Give the extent of all Plasmodium malariae-infected red blood cells.
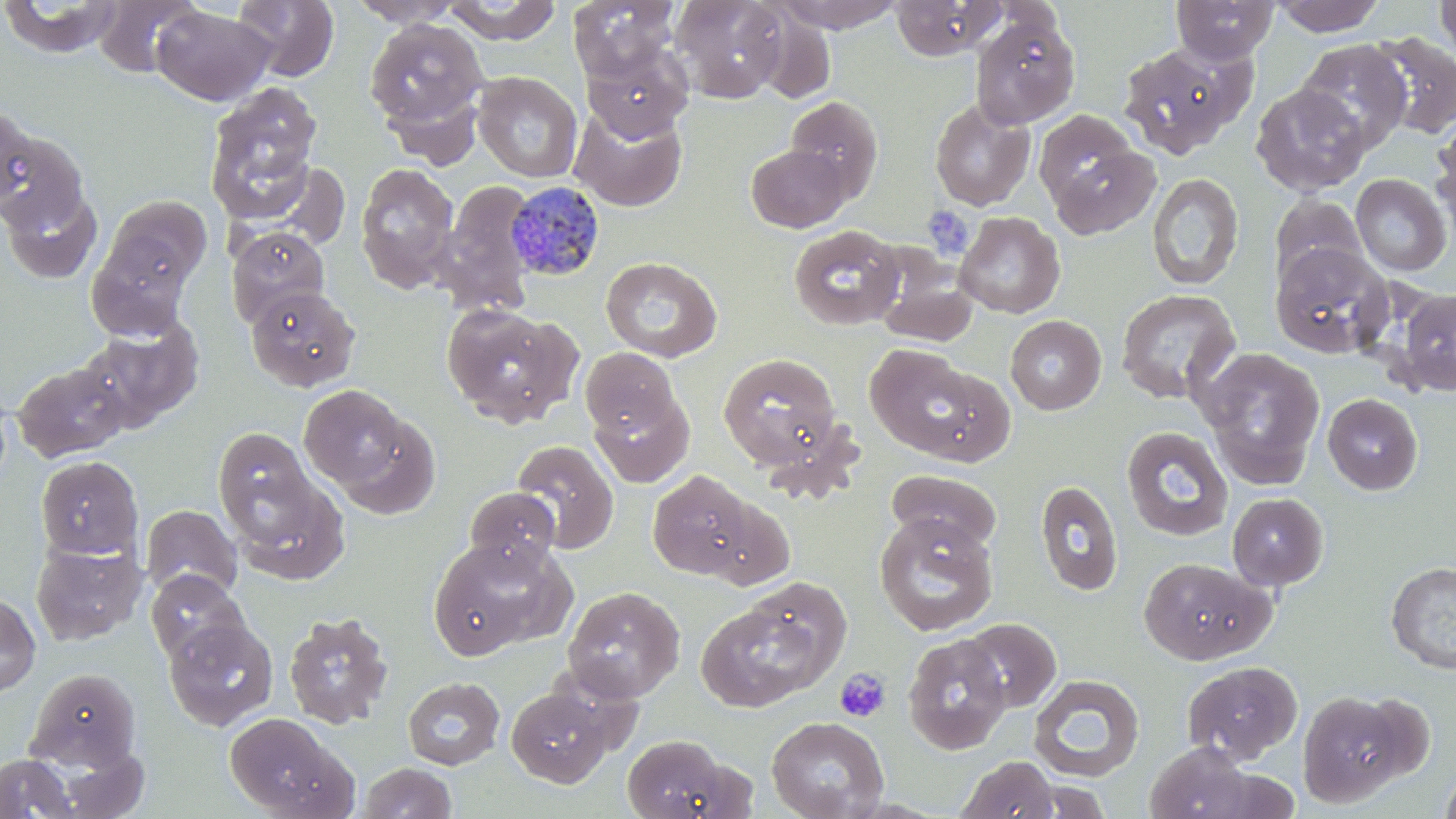
Approximate bounding boxes as (x1,y1)-(x2,y2) corner pairs in pixels.
Plasmodium malariae-infected red blood cells: (506,181)-(605,282).

Platelet locations: (833,667)-(891,724). Uninfected red blood cell locations: (0,0)-(124,59), (92,0)-(203,77), (233,0)-(339,82), (347,0)-(464,28), (568,0)-(679,83), (670,0)-(790,103), (769,0)-(907,32), (890,0)-(1004,61), (1172,0)-(1279,63), (1271,0)-(1386,36), (1433,0)-(1456,61), (443,1)-(563,44), (152,5)-(275,105), (970,12)-(1080,129), (364,19)-(487,134), (1367,31)-(1456,140), (1117,40)-(1253,160), (1295,40)-(1412,153), (582,43)-(692,142), (473,72)-(582,182), (204,82)-(324,226), (1250,83)-(1371,197), (785,95)-(883,200), (930,98)-(1035,211), (569,102)-(687,211), (0,104)-(39,216), (1433,115)-(1456,234), (0,126)-(91,239), (1044,139)-(1161,242), (746,144)-(851,232), (354,162)-(460,293), (268,163)-(353,249), (1146,172)-(1244,291), (1351,174)-(1452,276), (436,180)-(538,315), (3,186)-(102,283), (1268,194)-(1368,289), (102,195)-(212,294), (954,212)-(1065,318), (788,225)-(904,331), (227,226)-(330,326), (86,238)-(192,341), (1270,241)-(1394,358), (601,256)-(722,362), (873,259)-(979,347), (246,284)-(360,392), (1115,288)-(1241,405), (1396,288)-(1456,396), (442,304)-(578,426), (1005,315)-(1106,415), (80,320)-(203,429), (866,345)-(983,458), (1198,347)-(1325,488), (581,348)-(681,440), (718,352)-(842,470), (12,361)-(130,463), (299,384)-(409,490), (591,391)-(693,488), (1322,393)-(1423,495), (334,414)-(442,520), (1121,426)-(1234,542), (213,427)-(316,534), (512,440)-(618,553), (35,455)-(144,559), (886,469)-(1002,553), (647,470)-(755,578), (230,473)-(349,583), (1035,479)-(1123,596), (464,486)-(561,572), (1227,492)-(1328,590), (699,494)-(794,590), (141,505)-(242,601), (874,513)-(998,636), (428,538)-(561,658), (31,539)-(146,646), (1138,557)-(1273,664), (1386,561)-(1456,674), (145,570)-(250,666), (562,586)-(685,702), (0,592)-(40,698), (696,592)-(839,711), (282,610)-(394,729), (163,618)-(278,732), (960,618)-(1061,712), (903,634)-(1011,755), (1181,661)-(1302,764), (26,667)-(141,772), (1029,674)-(1145,782), (402,676)-(505,770), (505,686)-(617,788), (1297,690)-(1411,807), (1354,693)-(1437,781), (224,712)-(354,819), (767,716)-(890,819), (622,734)-(739,819), (1144,741)-(1258,819), (0,753)-(78,819), (956,755)-(1059,819), (357,762)-(459,818), (1439,764)-(1456,819), (1023,777)-(1112,818). Slide-level diagnosis: Plasmodium malariae. Captured at 1000x magnification. May-Grünwald-Giemsa stain. Image is 1456×819 pixels. One field of a larger specimen. Light microscopy. Thin blood smear.